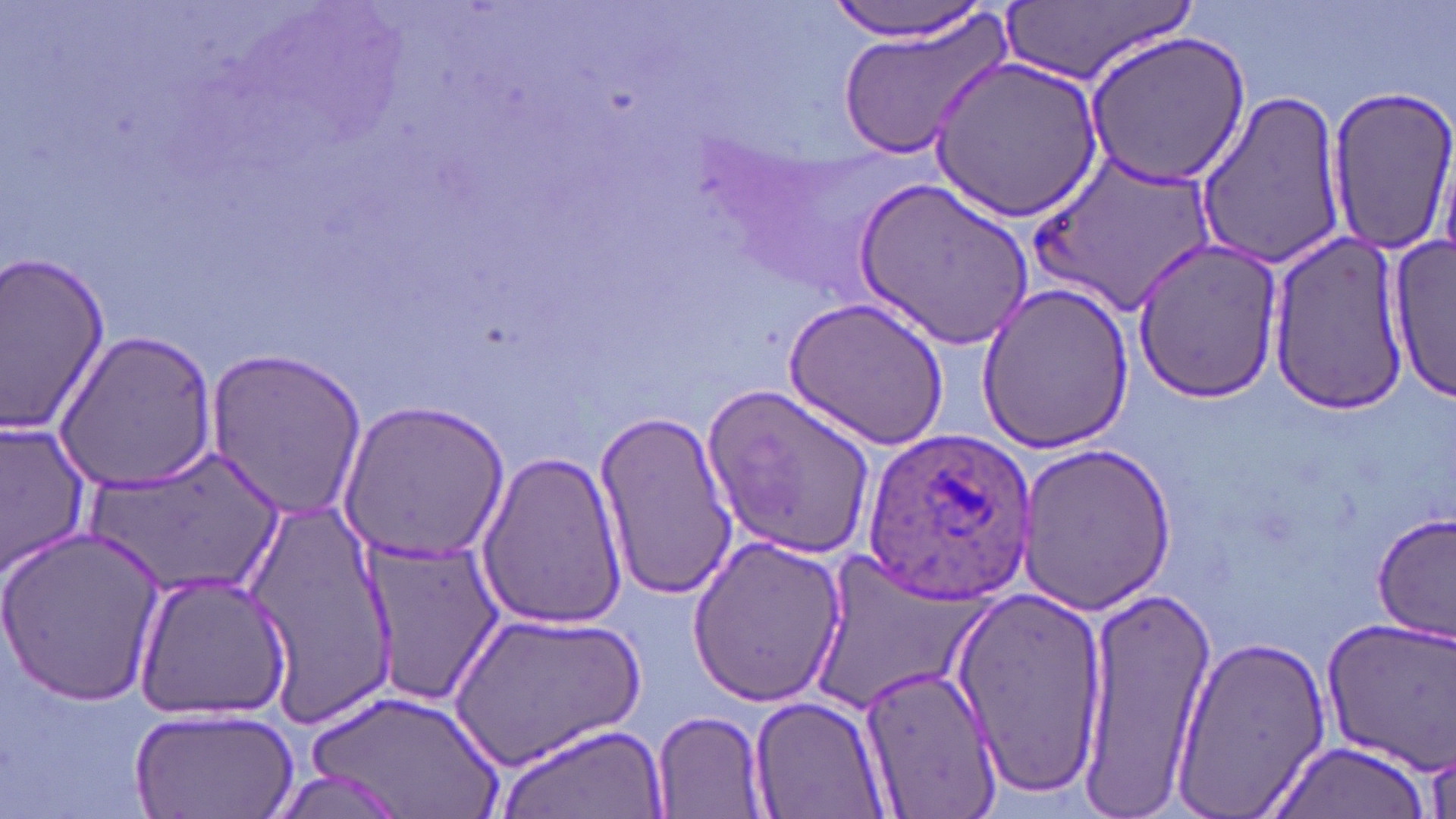

Summary:
  - Coordinate format: approximate bounding boxes as [x1, y1, x2, y2] in pixels
  - Uninfected red blood cell locations: [826, 0, 998, 44], [1000, 0, 1193, 89], [833, 11, 1014, 161], [1082, 29, 1251, 188], [929, 56, 1105, 224], [1324, 85, 1456, 258], [1194, 88, 1347, 269], [1036, 153, 1218, 314], [857, 179, 1034, 350], [1267, 230, 1412, 416], [1129, 240, 1285, 405], [1385, 240, 1455, 404], [0, 248, 114, 442], [975, 280, 1136, 455], [785, 295, 950, 452], [54, 328, 219, 494], [202, 350, 371, 520], [701, 387, 878, 558], [337, 400, 507, 568], [592, 409, 739, 599], [1, 419, 94, 577], [1014, 442, 1180, 613], [85, 444, 289, 603], [473, 449, 630, 630], [243, 492, 401, 723], [1372, 513, 1455, 643], [0, 527, 166, 704], [685, 533, 848, 706], [360, 538, 504, 706], [802, 554, 992, 719], [133, 568, 293, 722], [1072, 583, 1211, 803], [948, 585, 1110, 793], [444, 609, 647, 771], [1319, 617, 1456, 773], [1171, 633, 1334, 816], [858, 662, 999, 813], [302, 689, 508, 819], [748, 693, 891, 818], [651, 708, 771, 817], [129, 709, 298, 819], [492, 722, 671, 819], [1266, 739, 1433, 819]
  - Plasmodium ovale-infected red blood cell locations: [863, 429, 1037, 604]
  - Slide-level diagnosis: Plasmodium ovale
  - Magnification: 1000x
  - Modality: optical microscopy
  - Preparation: thin blood film
  - Image size: 1456×819 pixels
  - Stain: May-Grünwald-Giemsa
  - Field of view: one of a larger specimen